Classify this cell by malaria status.
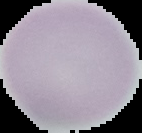

Uninfected.

Summary:
  - Image size: 142×133 pixels
  - Preparation: thin blood smear
  - Image type: segmented cell region on a black background